Classify this cell by malaria status.
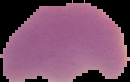

Parasitized.

Summary:
  - Image type: cell region segmented out of the field of view; surrounding area masked to black
  - Image size: 130×82 pixels
  - Preparation: thin blood film